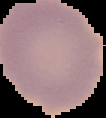

Summary:
  - Preparation: thin blood smear
  - Result: negative for Plasmodium parasites
  - Image size: 106×118 pixels
  - Image type: segmented cell region with the area outside set to black